Assess this cell for malaria.
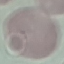

It is uninfected.

Summary:
  - Preparation: thin blood film
  - Image type: cell patch, automatically extracted from a larger field of view and resized to 64 × 64 pixels
  - Capture: smartphone camera at the microscope eyepiece
  - Stain: Giemsa